Classify this cell by malaria status.
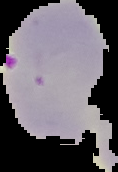

Parasitized.

preparation = thin blood smear
image size = 118×172 pixels
image type = segmented cell region on a black background